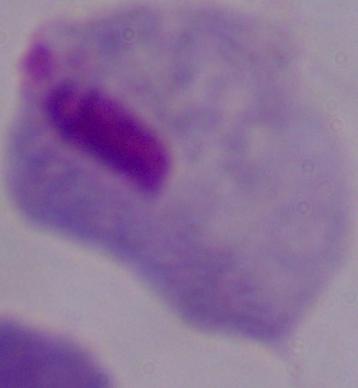

Summary:
  - Modality: photomicrograph
  - Magnification: 1000x
  - Identification: trichomonad